Assess the morphology of the red blood cells.
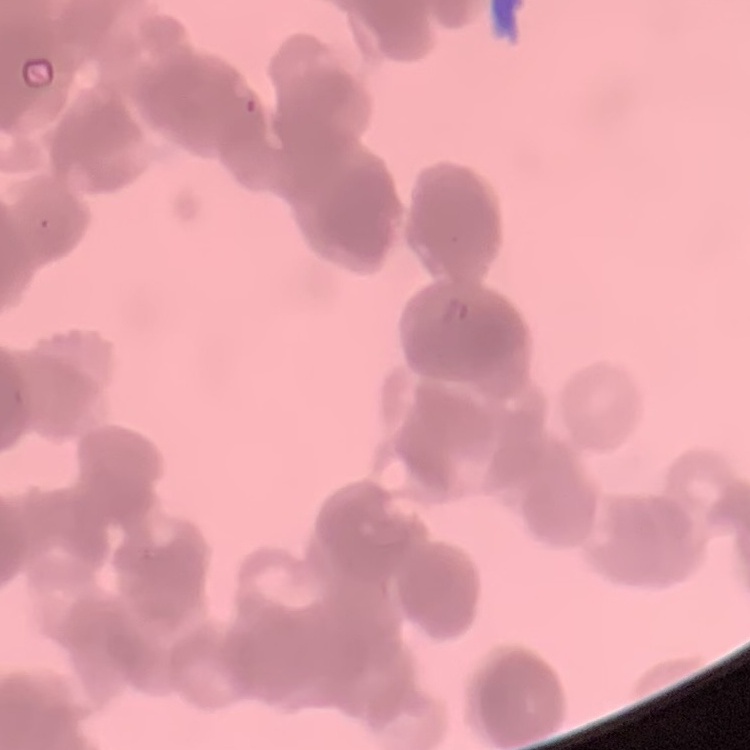
Rouleaux formation.

preparation = thin blood film
stain = Field's or Giemsa
image type = one tile cut from a larger photomicrograph